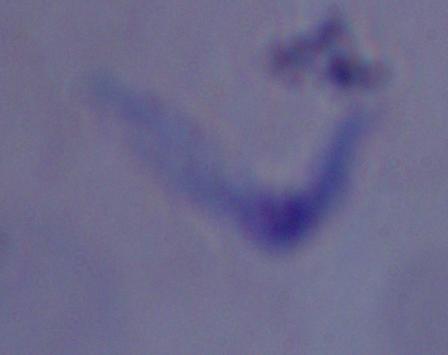
magnification: 1000x
identification: trypanosome
modality: micrograph